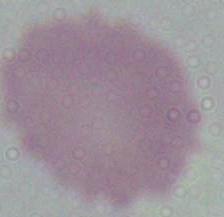

Summary:
  - Modality: micrograph
  - Magnification: 1000x
  - Identification: red blood cell